Comment on the morphology of the erythrocytes.
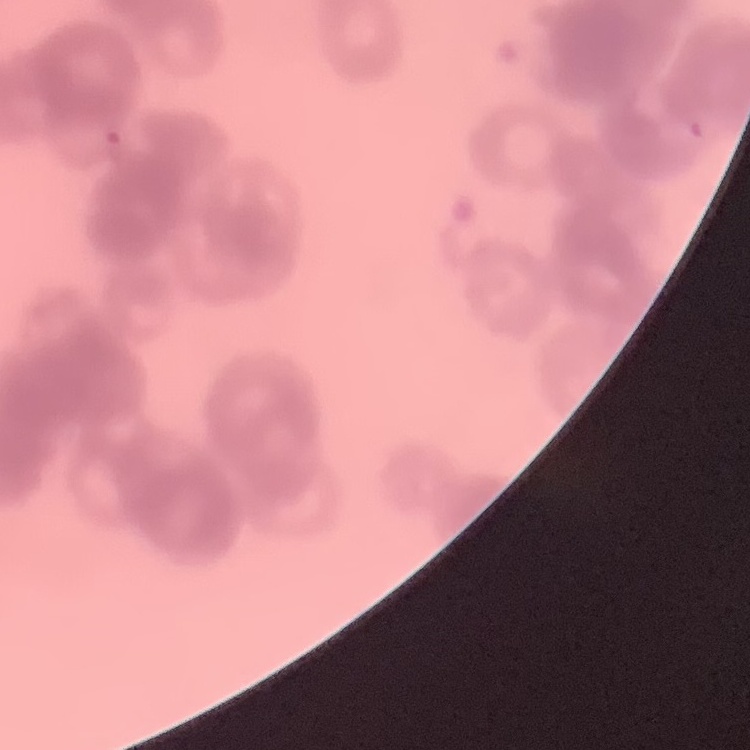
Rouleaux formation.

Summary:
  - Image type: square crop of a larger photomicrograph
  - Stain: Field's or Giemsa
  - Preparation: thin blood smear